Report the malaria status of this cell.
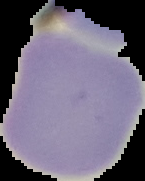
Uninfected.

{
  "preparation": "thin blood smear",
  "image_type": "cell region segmented out of the field of view; surrounding area masked to black",
  "image_size": "145×181 pixels"
}